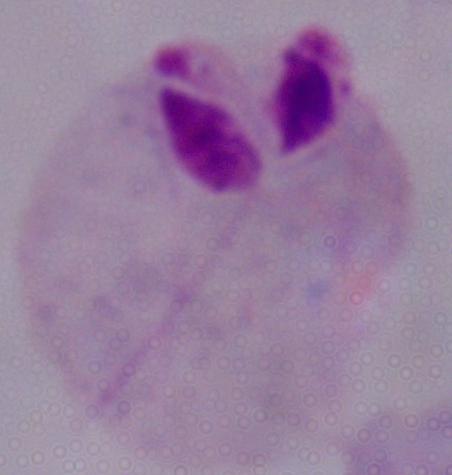
identification = trichomonad
magnification = 1000x
modality = photomicrograph